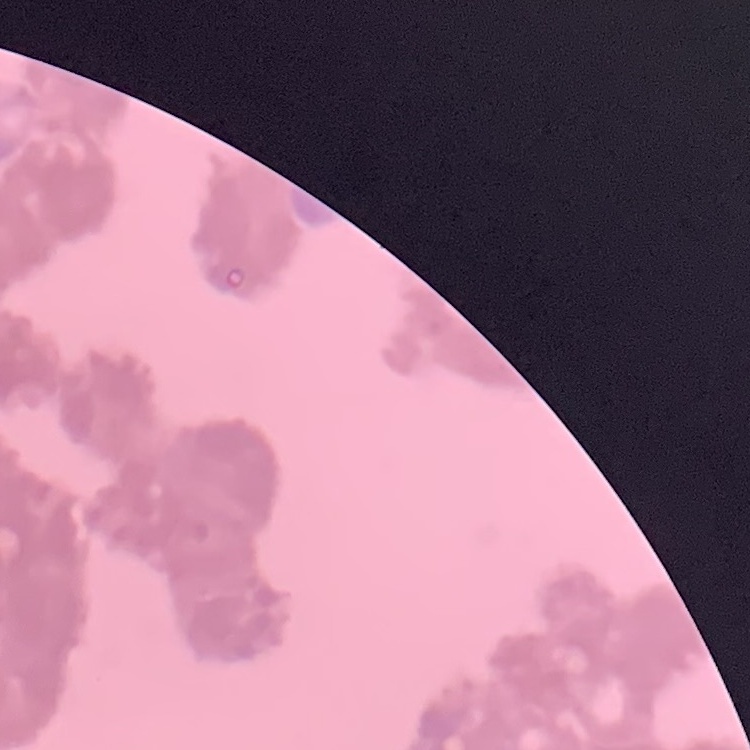

{
  "erythrocyte_morphology": "rouleaux formation",
  "preparation": "thin blood smear",
  "image_type": "square crop of a larger photomicrograph",
  "stain": "Field's or Giemsa"
}